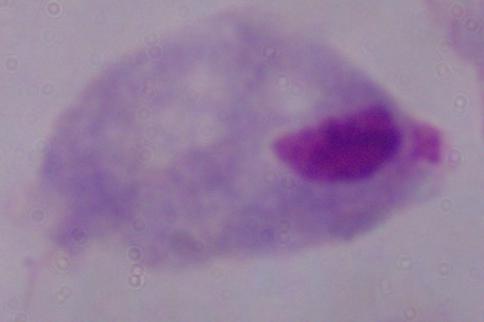
{
  "modality": "photomicrograph",
  "identification": "trichomonad",
  "magnification": "1000x"
}